Report the malaria status of this cell.
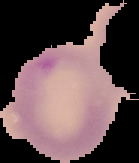
Parasitized.

preparation: thin blood smear
image_size: 139×163 pixels
image_type: segmented cell region on a black background